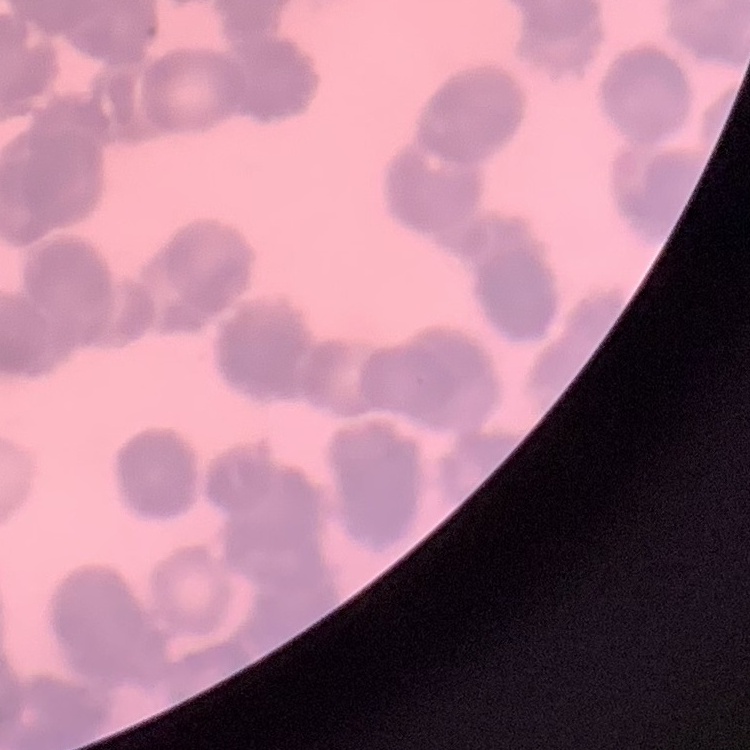 The erythrocytes show rouleaux formation. Thin peripheral smear. One tile cut from a larger photomicrograph. Field's or Giemsa stain.